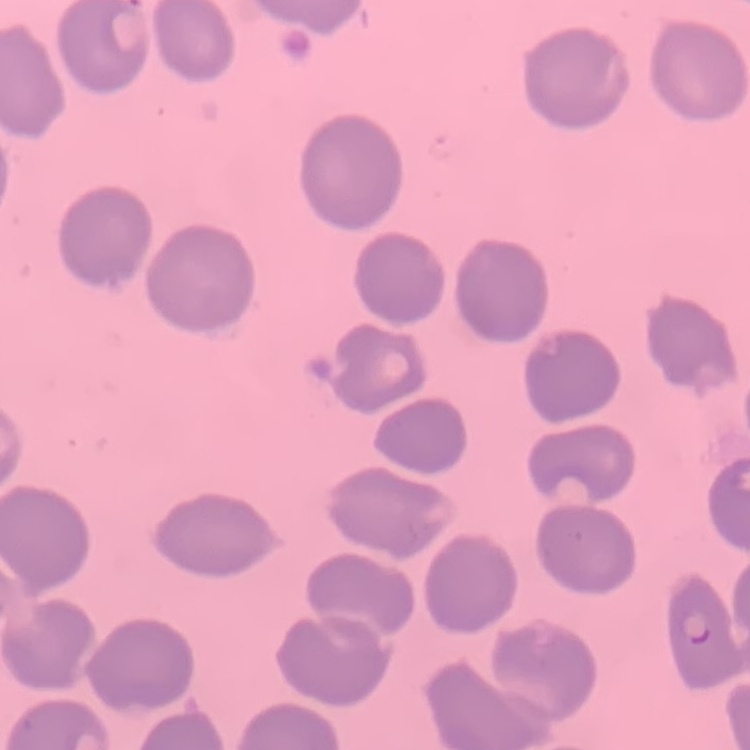
Summary:
  - Red blood cell morphology: no rouleaux formation
  - Image type: square crop of a larger photomicrograph
  - Stain: Field's or Giemsa
  - Preparation: thin blood film